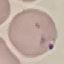
Malaria status: parasitized. Thin smear of blood. Photographed with a smartphone camera at the microscope eyepiece. Cell patch, automatically extracted from a larger field of view and resized to 64 × 64 pixels. Giemsa stain.